Assess this cell for malaria.
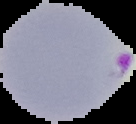
It is parasitized.

image type = cell region segmented out of the field of view; surrounding area masked to black
image size = 136×124 pixels
preparation = thin blood film